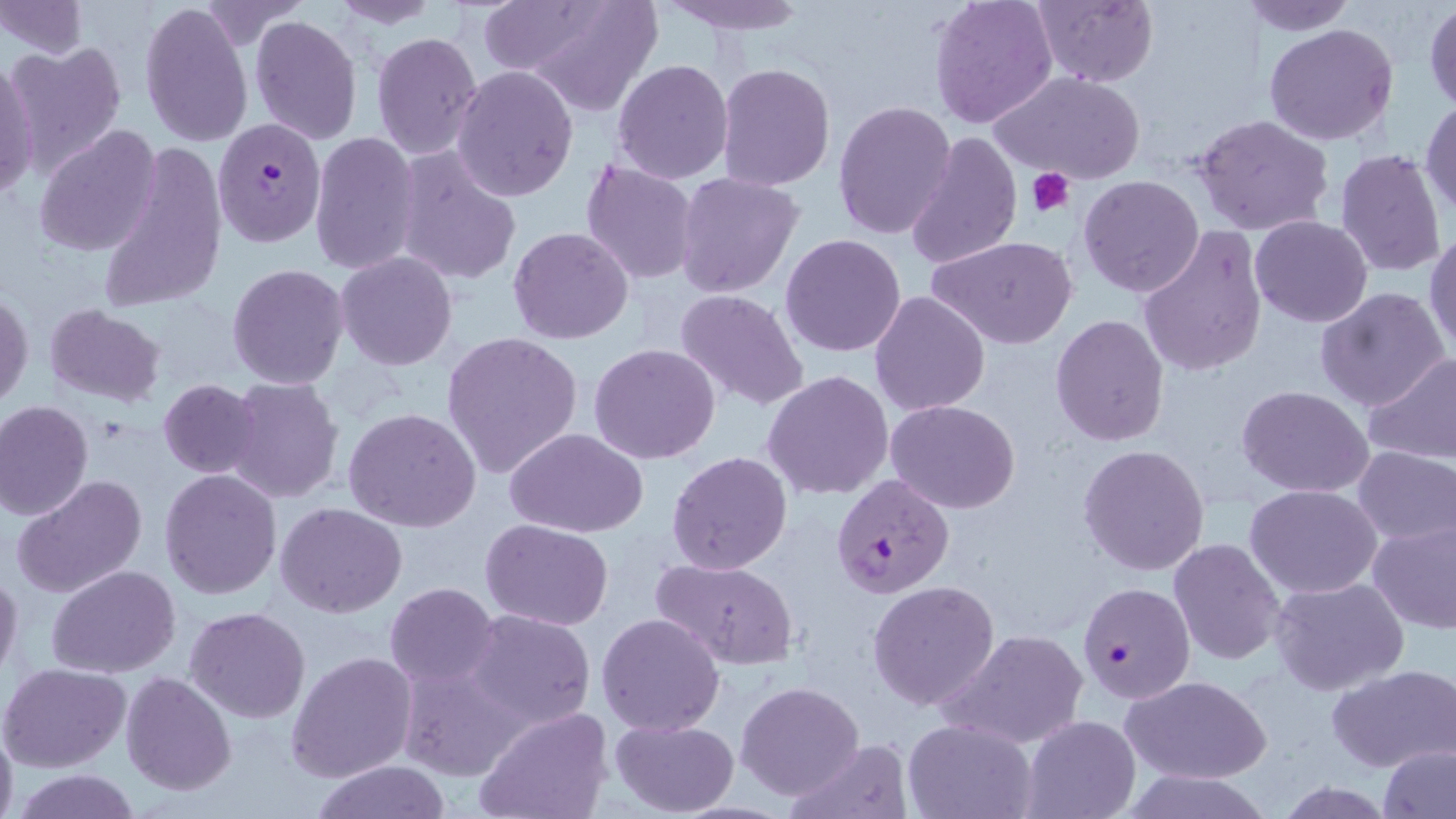

Summary:
  - Coordinate format: approximate bounding boxes as (x1,y1)-(x2,y2) corner pairs in pixels
  - Platelet locations: (1027,167)-(1076,219)
  - Plasmodium falciparum-infected red blood cell locations: (213,123)-(325,246), (831,475)-(955,600), (1078,581)-(1194,703)
  - Uninfected red blood cell locations: (503,0)-(664,114), (656,0)-(809,35), (929,0)-(1058,128), (1034,0)-(1159,88), (1236,0)-(1359,35), (0,1)-(86,60), (140,1)-(253,150), (328,1)-(440,28), (1424,1)-(1456,113), (195,3)-(308,51), (249,16)-(362,145), (1264,23)-(1398,147), (371,31)-(483,160), (6,44)-(125,171), (0,58)-(42,197), (613,59)-(733,183), (716,62)-(836,190), (451,65)-(578,201), (992,70)-(1144,185), (1420,99)-(1456,223), (832,100)-(956,241), (1192,115)-(1336,238), (34,124)-(162,257), (309,130)-(421,275), (904,130)-(1021,270), (99,143)-(226,311), (394,149)-(522,288), (1334,149)-(1447,279), (579,160)-(700,284), (675,172)-(804,297), (1078,174)-(1204,298), (1249,216)-(1373,327), (507,227)-(635,345), (1137,228)-(1266,377), (1426,231)-(1456,359), (780,234)-(907,357), (929,237)-(1077,350), (336,252)-(456,371), (226,263)-(349,391), (1316,287)-(1451,412), (675,288)-(809,412), (869,291)-(990,418), (1,293)-(33,409), (45,304)-(167,408), (1050,314)-(1171,447), (440,331)-(585,478), (589,344)-(720,465), (1362,353)-(1456,465), (762,370)-(893,499), (224,376)-(344,504), (158,378)-(262,477), (1236,385)-(1374,497), (0,400)-(93,520), (887,400)-(1021,514), (343,407)-(482,532), (504,427)-(649,538), (1079,444)-(1209,577), (1355,446)-(1455,547), (666,450)-(793,576), (159,469)-(284,600), (12,473)-(148,598), (1247,483)-(1382,598), (276,502)-(407,619), (480,517)-(614,631), (1367,519)-(1456,635), (1168,539)-(1284,665), (651,557)-(800,671), (48,565)-(181,679), (0,567)-(23,683), (1270,576)-(1407,695), (867,580)-(1000,709), (386,582)-(499,690), (185,607)-(310,724), (463,608)-(597,731), (596,612)-(726,737), (938,627)-(1087,748), (285,650)-(416,782), (396,658)-(530,783), (0,661)-(130,771), (1327,663)-(1455,772), (120,671)-(236,796), (1119,675)-(1270,784), (736,680)-(865,800), (475,708)-(612,819), (1022,715)-(1139,818), (611,718)-(740,817), (903,718)-(1037,819), (0,724)-(18,819), (786,737)-(913,818), (1377,743)-(1454,818), (312,760)-(453,819), (14,769)-(142,819)
  - Slide-level diagnosis: Plasmodium falciparum
  - Field of view: single
  - Preparation: thin blood smear
  - Modality: light microscopy
  - Magnification: 1000x
  - Image size: 1456×819 pixels
  - Stain: May-Grünwald-Giemsa